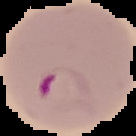

malaria status = parasitized
image type = cell region segmented out of the field of view; surrounding area masked to black
preparation = thin blood smear
image size = 136×136 pixels